Classify this cell by malaria status.
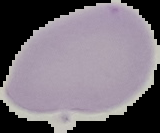
It is uninfected.

From a thin blood film. The area outside the segmented cell region is set to black. Image is 160×133 pixels.